Report the malaria status of this cell.
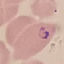

Parasitized.

{
  "stain": "Giemsa",
  "preparation": "thin blood smear",
  "capture": "smartphone through the microscope eyepiece",
  "image_type": "automatically extracted cell patch, resized to 64 × 64 pixels"
}